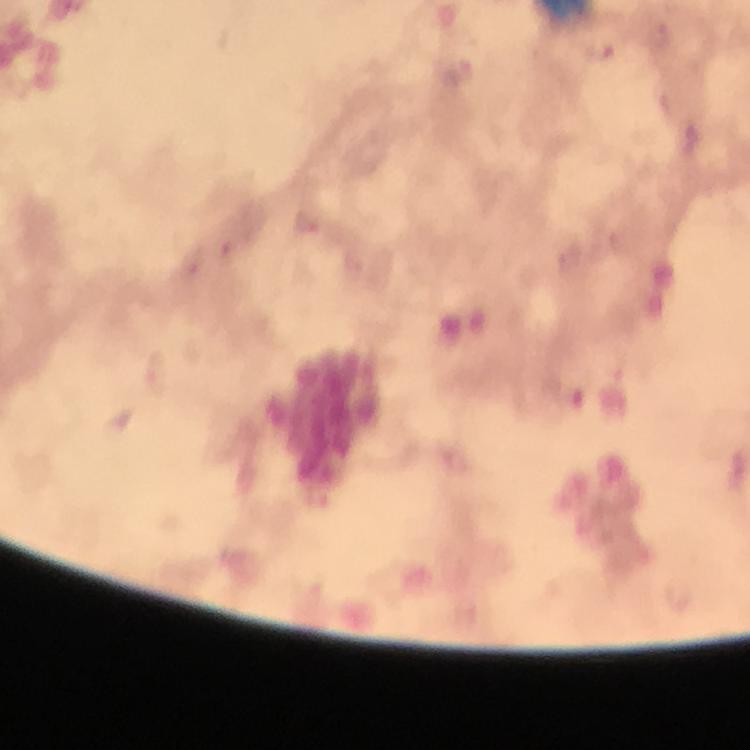

Approximate object centers, in pixels from the top-left corner.
Summary:
  - Malaria parasite locations: (x=599, y=52)
  - Capture: smartphone mounted on the microscope
  - Preparation: thick blood smear
  - Magnification: 100x
  - Context: from a malaria diagnostic workup
  - Image size: 750×750 pixels
  - Immersion oil: used
  - Stain: Giemsa
  - Cropped from: a single field of view